Name the blood parasite species.
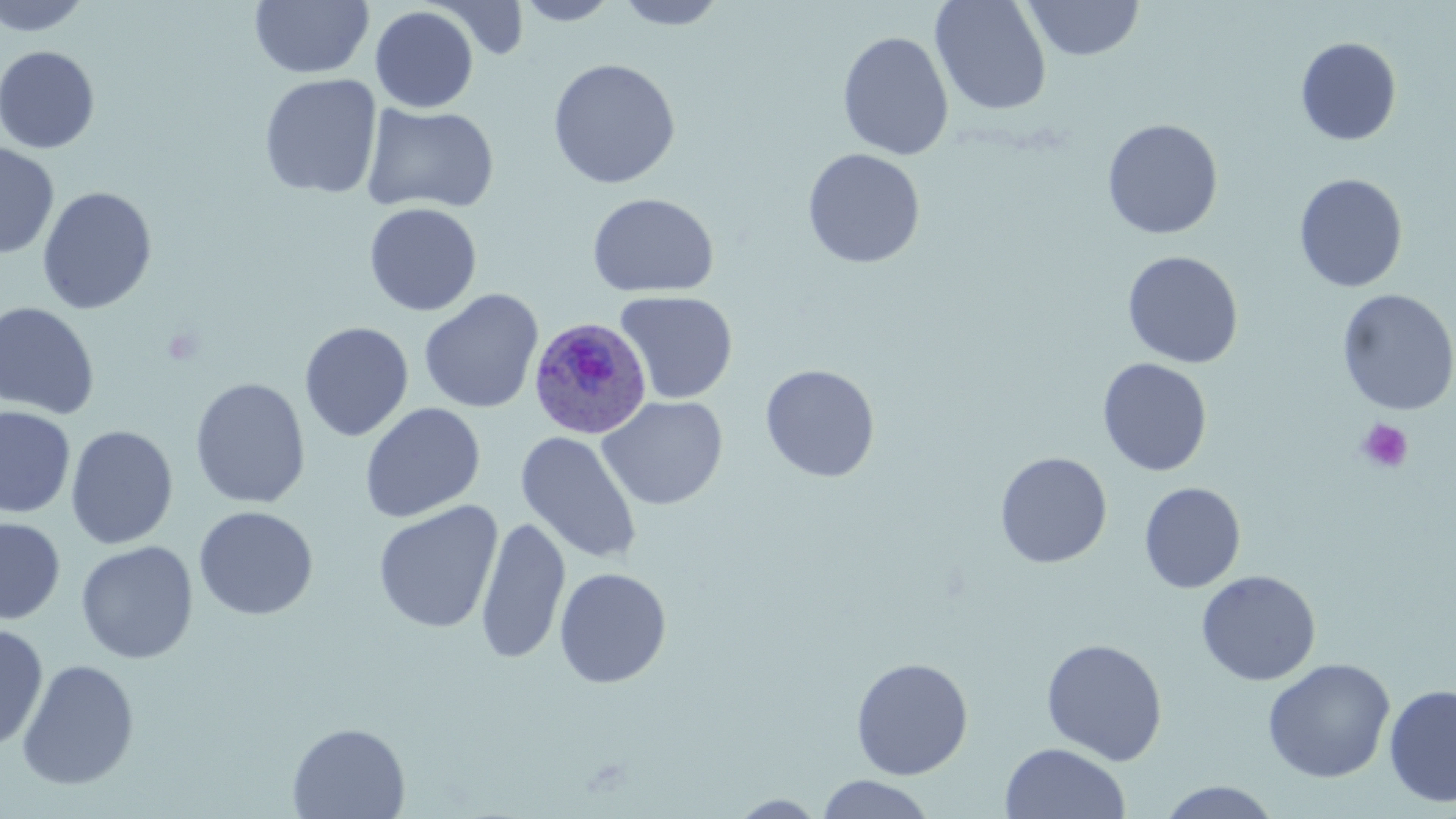

Plasmodium ovale.

Approximate bounding boxes as (x1,y1)-(x2,y2) corner pairs in pixels. Plasmodium ovale-infected red blood cell locations: (528,317)-(652,440). Uninfected red blood cell locations: (0,0)-(93,36), (250,0)-(374,79), (513,0)-(622,25), (612,0)-(730,30), (930,0)-(1052,117), (1024,0)-(1145,60), (431,1)-(530,59), (370,5)-(479,113), (837,30)-(954,161), (1295,37)-(1402,145), (0,45)-(101,154), (547,58)-(681,189), (259,74)-(382,199), (361,103)-(500,215), (1101,117)-(1223,240), (0,142)-(59,259), (802,148)-(925,269), (1294,173)-(1408,292), (37,186)-(158,315), (586,192)-(720,298), (364,202)-(483,316), (1122,250)-(1244,369), (1336,288)-(1455,416), (419,289)-(544,414), (615,290)-(738,404), (0,301)-(100,419), (299,321)-(414,442), (1097,357)-(1213,477), (760,363)-(881,483), (189,378)-(311,509), (597,396)-(728,510), (360,402)-(486,523), (0,406)-(76,518), (65,425)-(179,549), (516,431)-(641,565), (994,451)-(1112,568), (1139,482)-(1246,593), (373,500)-(504,635), (193,505)-(319,621), (475,515)-(570,665), (0,517)-(65,625), (75,540)-(198,664), (554,567)-(672,689), (1196,570)-(1321,686), (0,623)-(49,751), (1040,638)-(1168,765), (850,657)-(973,780), (1262,658)-(1395,783), (16,659)-(140,790), (1383,683)-(1456,808), (287,722)-(411,818), (999,742)-(1130,819), (816,774)-(936,818), (1155,781)-(1283,818), (728,793)-(828,817). Platelet locations: (1356,418)-(1414,474). One field of a larger specimen. Thin blood film. Image is 1456×819 pixels. Optical microscopy. 1000x magnification. May-Grünwald-Giemsa stain.